Describe the morphology of the erythrocytes.
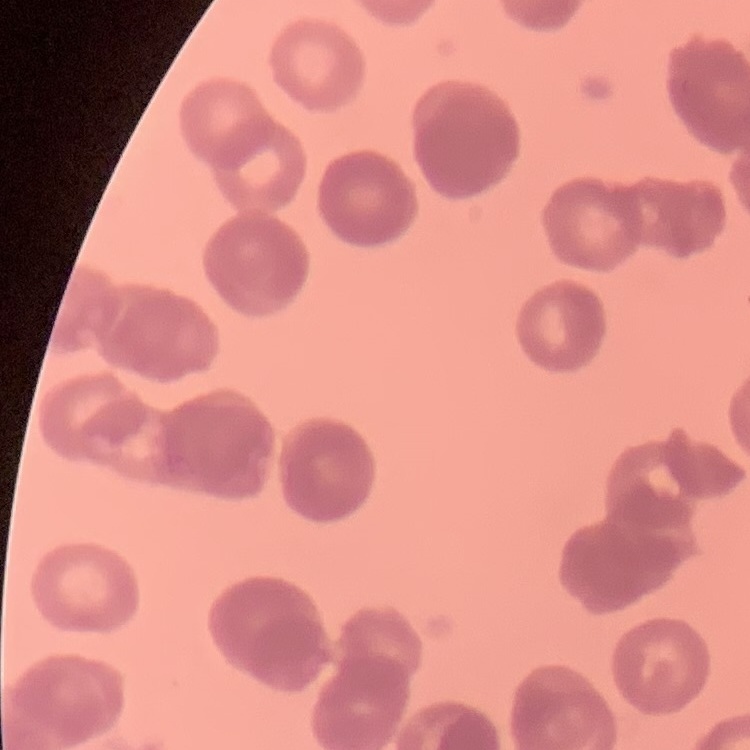
Rouleaux formation.

image type = one tile cut from a larger photomicrograph
stain = Field's or Giemsa
preparation = thin blood smear